Outline each Plasmodium falciparum-infected red blood cell.
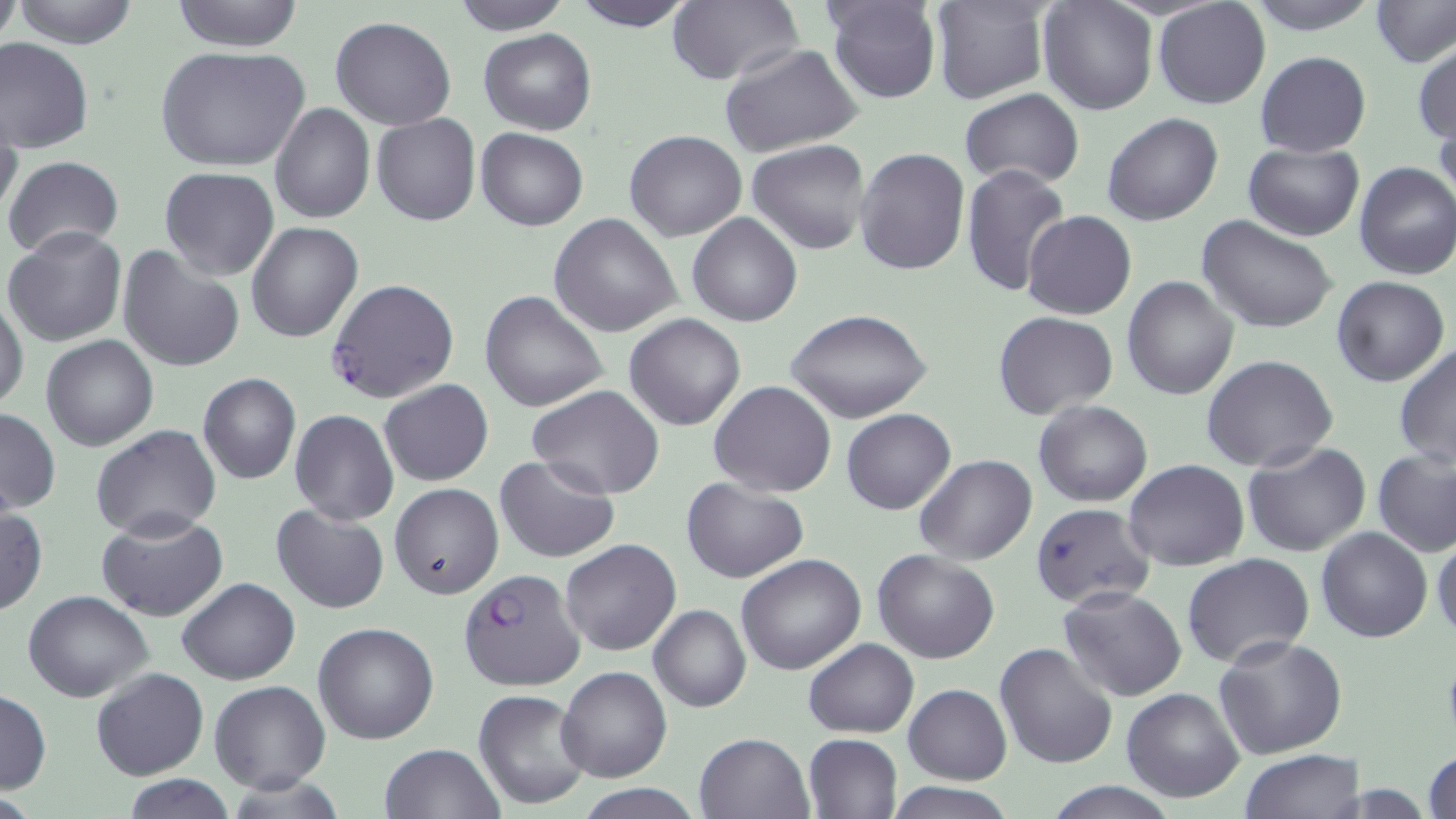

Approximate bounding boxes as (x1, y1, x2, y2) in pixels.
Plasmodium falciparum-infected red blood cells: (326, 278, 459, 404), (457, 567, 585, 692).

slide_level_diagnosis: Plasmodium falciparum
image_size: 1456×819 pixels
uninfected_red_blood_cell_locations: 'approximate bounding boxes as (x1, y1, x2, y2) in pixels: (1, 0, 18, 57), (12, 0, 141, 48), (170, 0, 306, 52), (568, 0, 698, 31), (668, 0, 805, 85), (825, 0, 942, 105), (930, 0, 1051, 105), (1244, 0, 1383, 34), (1373, 0, 1455, 67), (452, 1, 570, 33), (1039, 1, 1156, 115), (1153, 1, 1271, 111), (330, 16, 457, 130), (479, 28, 596, 135), (0, 37, 95, 153), (1413, 39, 1456, 145), (718, 43, 864, 161), (157, 45, 310, 174), (1255, 51, 1371, 156), (960, 87, 1085, 189), (270, 103, 375, 222), (0, 110, 22, 228), (372, 113, 481, 226), (1101, 113, 1222, 226), (475, 128, 589, 231), (624, 128, 746, 242), (748, 139, 872, 254), (1242, 142, 1363, 240), (854, 147, 971, 276), (3, 155, 125, 256), (1352, 162, 1456, 280), (961, 163, 1071, 297), (160, 167, 279, 280), (1023, 209, 1136, 320), (688, 212, 802, 326), (549, 215, 682, 337), (1197, 215, 1337, 333), (245, 221, 363, 342), (4, 226, 128, 348), (117, 244, 247, 373), (499, 252, 652, 395), (1123, 275, 1240, 400), (1331, 276, 1449, 386), (478, 290, 608, 412), (0, 295, 26, 412), (788, 311, 932, 423), (993, 311, 1119, 421), (624, 313, 746, 431), (41, 334, 160, 452), (1394, 344, 1455, 468), (1201, 355, 1339, 473), (198, 373, 301, 485), (379, 379, 493, 486), (708, 381, 836, 497), (526, 384, 665, 499), (1034, 400, 1153, 507), (1, 406, 60, 514), (840, 408, 956, 514), (289, 409, 399, 525), (90, 424, 222, 540), (1242, 441, 1372, 556), (1373, 449, 1455, 558), (493, 454, 621, 563), (914, 454, 1036, 565), (1124, 458, 1248, 570), (682, 477, 809, 582), (389, 483, 503, 599), (1030, 502, 1156, 609), (271, 504, 390, 614), (0, 507, 46, 614), (97, 511, 228, 621), (1316, 525, 1433, 642), (1431, 535, 1456, 643), (561, 538, 681, 656), (872, 549, 1000, 663), (736, 553, 867, 675), (1182, 553, 1314, 669), (177, 577, 299, 684), (1058, 586, 1187, 700), (23, 590, 153, 702), (648, 605, 750, 712), (313, 621, 439, 744), (1215, 634, 1349, 758), (804, 638, 918, 737), (993, 641, 1118, 769), (555, 665, 671, 782), (91, 667, 209, 780), (209, 680, 331, 793), (903, 684, 1013, 784), (1122, 687, 1247, 802), (0, 689, 51, 794), (473, 689, 593, 811), (693, 732, 813, 819), (803, 732, 903, 818), (377, 742, 505, 819), (1424, 746, 1456, 819), (1240, 749, 1363, 818), (120, 775, 238, 817), (882, 779, 1023, 819), (1041, 779, 1183, 818), (573, 785, 709, 818)'
modality: optical microscopy
field_of_view: single
preparation: thin blood film
magnification: 1000x
stain: May-Grünwald-Giemsa